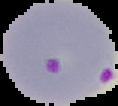

image size = 118×106 pixels
malaria status = parasitized
preparation = thin blood smear
image type = segmented cell region on a black background